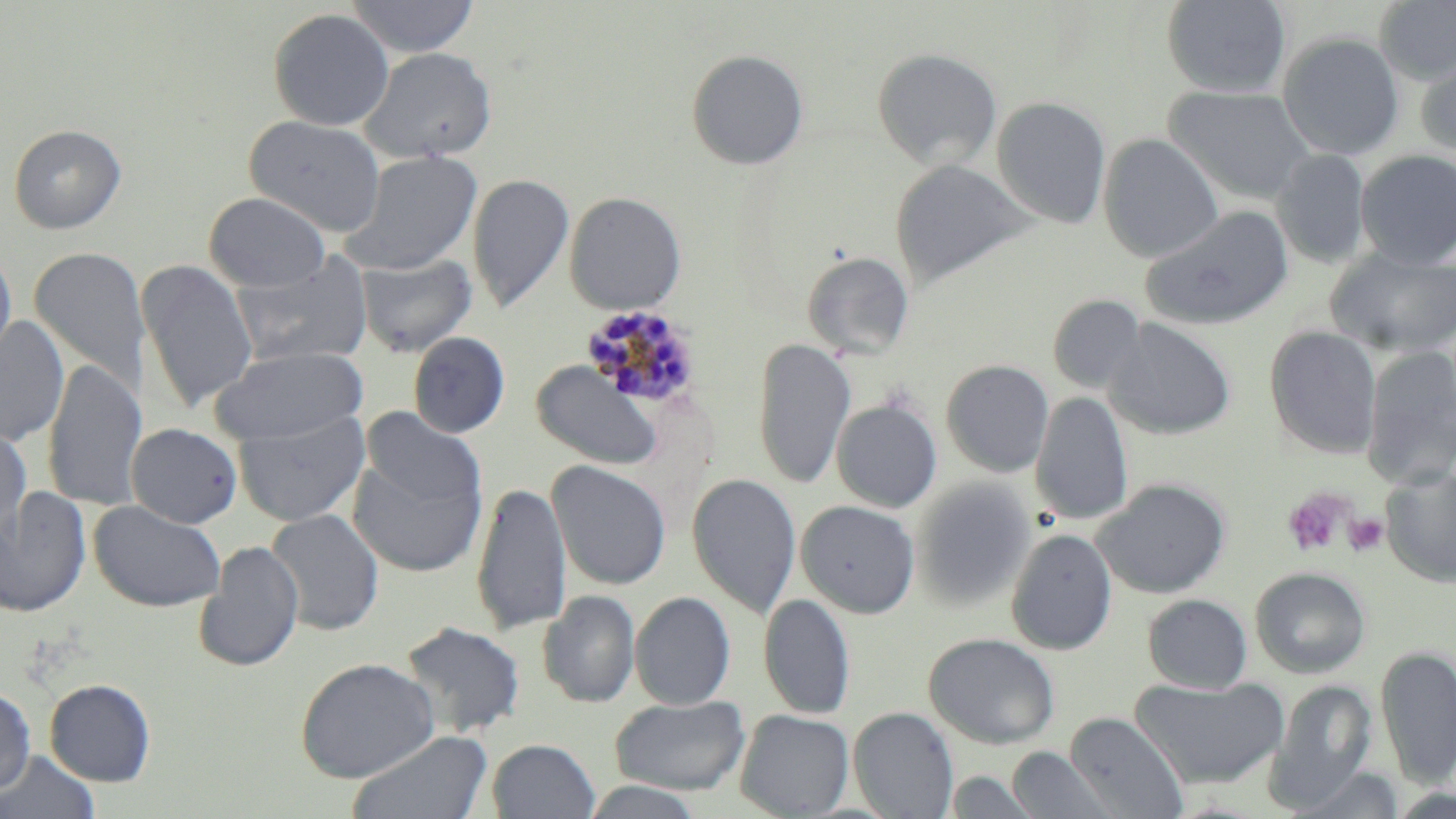
Summary:
  - Coordinate format: approximate bounding boxes as [x1, y1, x2, y2] in pixels
  - Uninfected red blood cell locations: [345, 0, 480, 58], [1161, 0, 1291, 99], [1374, 0, 1456, 85], [267, 8, 395, 131], [1277, 31, 1404, 160], [360, 46, 498, 164], [872, 47, 1003, 171], [686, 49, 809, 170], [1415, 50, 1456, 161], [1165, 84, 1317, 205], [991, 96, 1111, 228], [245, 114, 386, 237], [8, 123, 126, 234], [1099, 133, 1222, 263], [1272, 149, 1371, 268], [341, 150, 483, 275], [1354, 150, 1456, 270], [891, 159, 1034, 290], [467, 173, 575, 314], [564, 191, 687, 314], [204, 193, 331, 292], [1139, 205, 1294, 332], [0, 246, 17, 375], [29, 247, 151, 397], [1326, 248, 1456, 358], [801, 251, 915, 359], [354, 252, 477, 358], [231, 253, 374, 368], [136, 260, 258, 412], [1048, 294, 1146, 394], [0, 315, 69, 447], [1103, 318, 1237, 440], [1263, 326, 1383, 459], [408, 332, 510, 438], [752, 337, 856, 490], [1361, 345, 1456, 489], [210, 346, 367, 446], [43, 358, 146, 511], [941, 359, 1054, 477], [532, 361, 662, 470], [1030, 391, 1133, 526], [831, 398, 942, 513], [359, 406, 487, 520], [233, 410, 370, 527], [0, 422, 31, 542], [125, 422, 243, 528], [348, 450, 483, 578], [547, 460, 671, 590], [1380, 466, 1456, 588], [687, 472, 802, 619], [912, 479, 1036, 611], [1093, 479, 1231, 599], [472, 481, 572, 636], [0, 487, 92, 618], [88, 500, 227, 612], [796, 500, 920, 618], [265, 508, 384, 636], [1005, 528, 1117, 655], [194, 541, 304, 672], [1250, 566, 1370, 679], [538, 590, 640, 708], [630, 591, 736, 709], [758, 593, 855, 719], [1142, 594, 1252, 693], [400, 620, 525, 738], [924, 632, 1060, 750], [1375, 646, 1456, 788], [295, 657, 440, 783], [1129, 675, 1288, 790], [45, 678, 157, 786], [1264, 678, 1376, 809], [0, 687, 36, 793], [611, 695, 750, 795], [848, 707, 958, 818], [735, 709, 854, 818], [1064, 711, 1189, 819], [348, 730, 493, 819], [487, 739, 600, 819], [1006, 746, 1117, 819], [0, 749, 101, 819], [1290, 764, 1406, 818], [944, 770, 1042, 818], [578, 780, 710, 819]
  - Plasmodium malariae-infected red blood cell locations: [582, 305, 703, 412]
  - Platelet locations: [1281, 487, 1356, 558], [1343, 514, 1387, 556]
  - Slide-level diagnosis: Plasmodium malariae
  - Magnification: 1000x
  - Stain: May-Grünwald-Giemsa
  - Preparation: thin blood film
  - Modality: optical microscopy
  - Field of view: single
  - Image size: 1456×819 pixels